Locate every Plasmodium ovale-infected red blood cell.
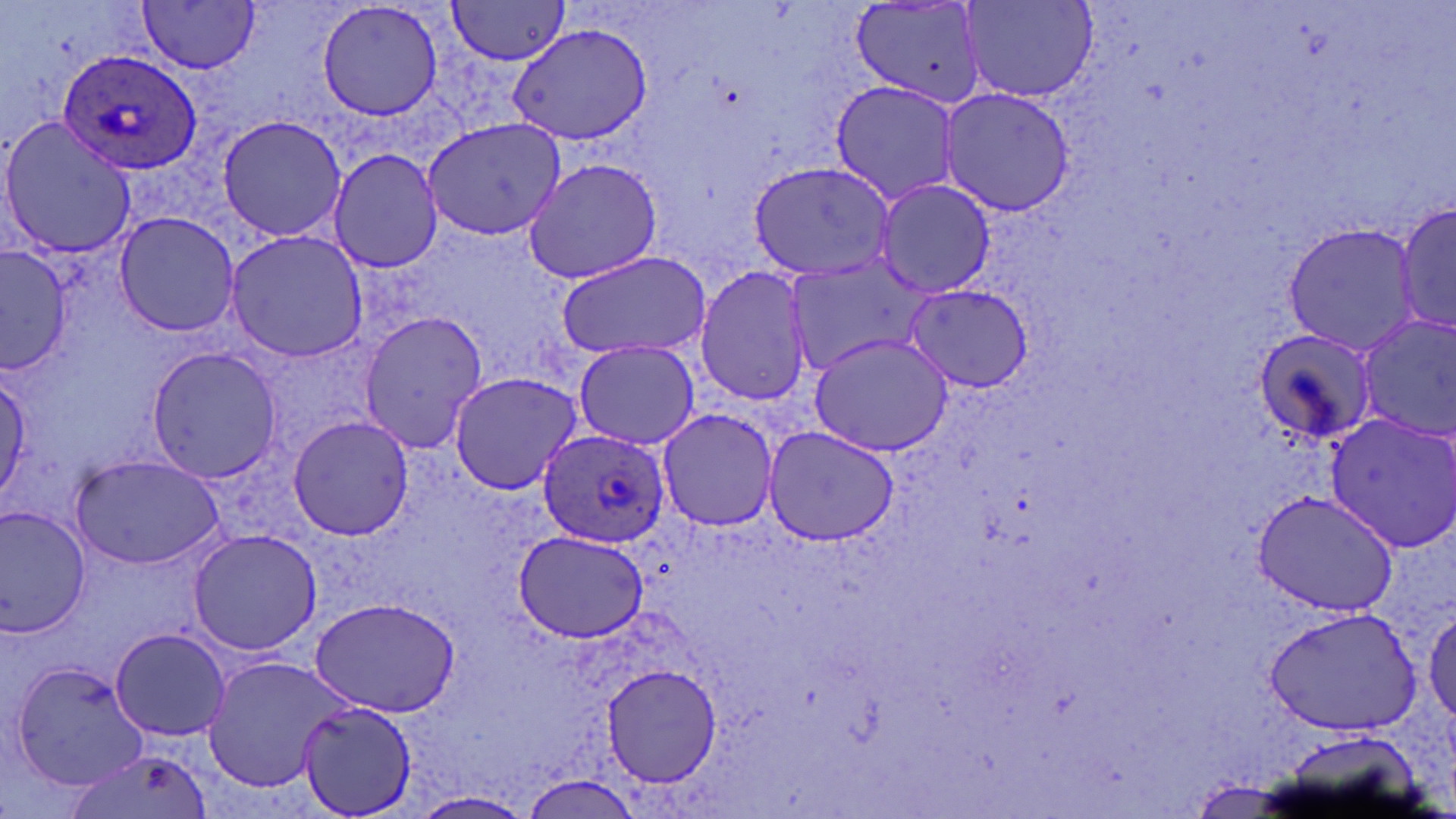
Approximate bounding boxes as (x1,y1)-(x2,y2) corner pairs in pixels.
Plasmodium ovale-infected red blood cells: (59,50)-(203,174), (538,430)-(668,546).

Uninfected red blood cell locations: (138,0)-(262,74), (315,0)-(445,121), (445,1)-(574,65), (962,1)-(1098,103), (849,3)-(988,109), (505,24)-(651,146), (828,79)-(962,206), (940,88)-(1075,214), (216,114)-(347,242), (0,118)-(136,262), (427,118)-(565,244), (325,148)-(446,275), (522,157)-(664,285), (748,162)-(894,280), (875,179)-(995,298), (1397,198)-(1456,342), (111,210)-(240,338), (1282,222)-(1422,355), (223,230)-(369,360), (0,245)-(73,373), (555,250)-(712,360), (783,256)-(930,371), (693,267)-(813,409), (904,284)-(1031,390), (357,311)-(488,455), (1349,315)-(1456,443), (1246,326)-(1379,449), (806,332)-(956,460), (574,339)-(700,450), (144,345)-(285,483), (0,367)-(33,505), (447,372)-(584,496), (655,410)-(780,532), (1323,410)-(1456,552), (285,416)-(415,540), (762,426)-(898,547), (69,453)-(226,569), (1250,489)-(1400,617), (1,504)-(94,636), (186,527)-(321,657), (512,530)-(652,642), (308,597)-(462,717), (1266,604)-(1424,737), (1424,605)-(1456,726), (109,626)-(230,742), (200,655)-(356,795), (14,660)-(151,791), (602,662)-(722,790), (300,702)-(416,816), (63,747)-(212,819), (521,776)-(642,816), (411,790)-(532,819). Slide-level diagnosis: Plasmodium ovale. One field of a larger specimen. May-Grünwald-Giemsa stain. 1000x magnification. Thin blood smear. Image is 1456×819 pixels. Optical microscopy.